Assess this cell for malaria.
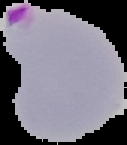

It is parasitized.

Summary:
  - Preparation: thin blood film
  - Image size: 127×145 pixels
  - Image type: cell region segmented out of the field of view; surrounding area masked to black